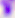

Captured at 400x magnification. Micrograph. Toxoplasma gondii is seen.